Comment on the morphology of the erythrocytes.
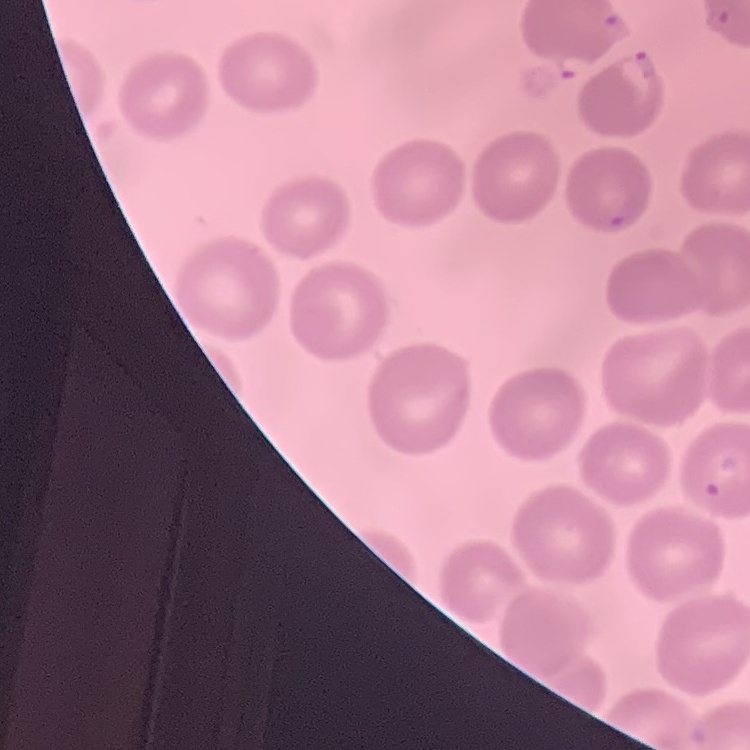

No rouleaux formation.

One tile cut from a larger photomicrograph. Thin blood film. Stained with either Field's or Giemsa.